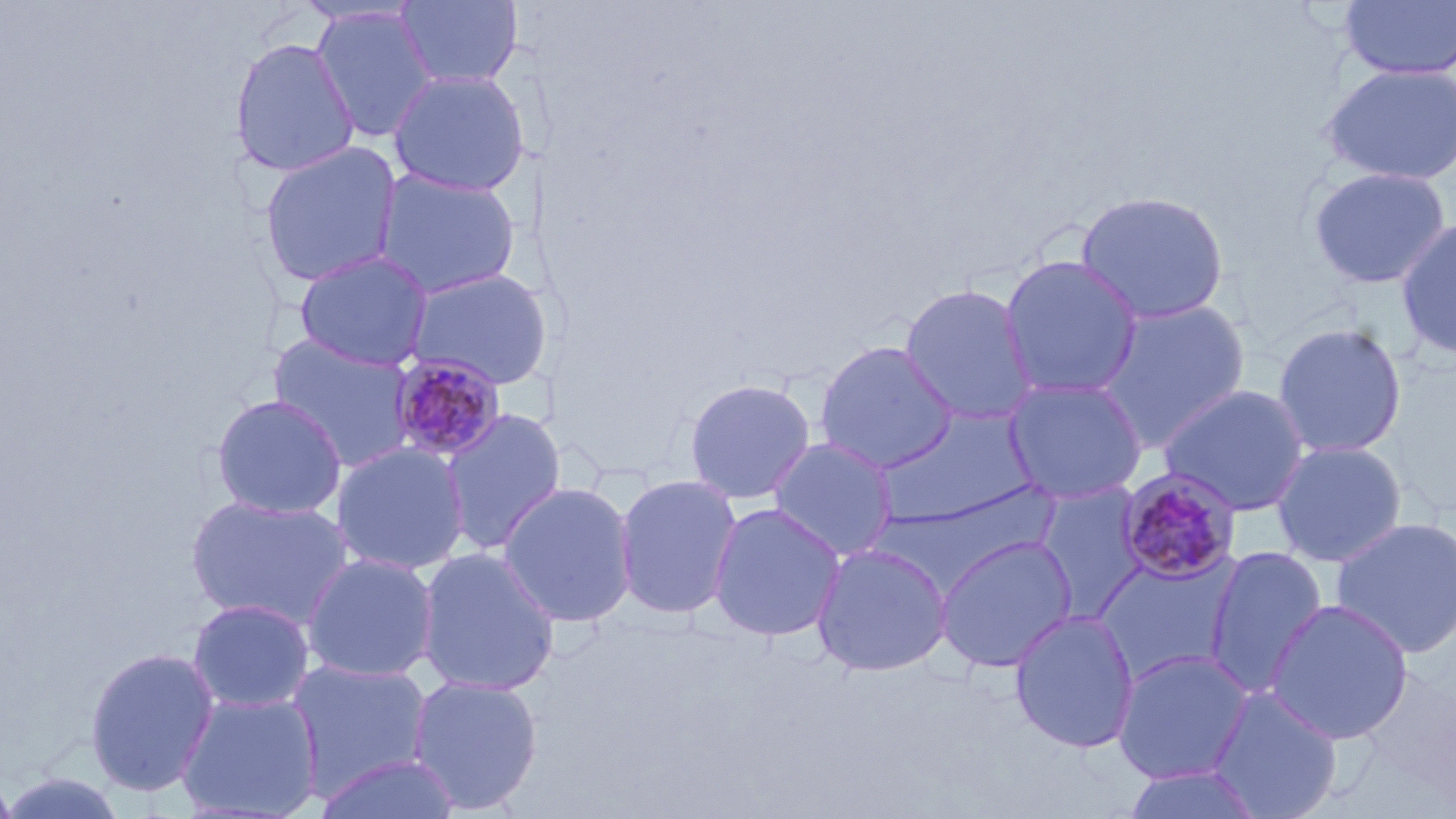
Approximate bounding boxes as named x1/y1/x2/y2 corners in pixels. Uninfected red blood cell locations: (x1=394, y1=0, x2=523, y2=89), (x1=1337, y1=1, x2=1456, y2=80), (x1=310, y1=6, x2=439, y2=143), (x1=228, y1=36, x2=359, y2=177), (x1=1318, y1=62, x2=1456, y2=186), (x1=388, y1=69, x2=530, y2=196), (x1=258, y1=141, x2=404, y2=287), (x1=1306, y1=166, x2=1453, y2=290), (x1=373, y1=168, x2=523, y2=300), (x1=1075, y1=190, x2=1230, y2=325), (x1=1395, y1=216, x2=1456, y2=360), (x1=293, y1=250, x2=434, y2=371), (x1=1000, y1=254, x2=1143, y2=400), (x1=402, y1=267, x2=551, y2=390), (x1=899, y1=283, x2=1039, y2=426), (x1=1095, y1=300, x2=1250, y2=450), (x1=1272, y1=321, x2=1408, y2=459), (x1=268, y1=332, x2=420, y2=472), (x1=815, y1=340, x2=958, y2=474), (x1=683, y1=377, x2=816, y2=504), (x1=1003, y1=378, x2=1147, y2=505), (x1=1158, y1=383, x2=1312, y2=516), (x1=211, y1=394, x2=347, y2=520), (x1=877, y1=406, x2=1038, y2=527), (x1=439, y1=408, x2=567, y2=555), (x1=768, y1=437, x2=899, y2=561), (x1=1271, y1=439, x2=1408, y2=567), (x1=331, y1=441, x2=470, y2=575), (x1=613, y1=473, x2=743, y2=619), (x1=498, y1=482, x2=638, y2=627), (x1=1033, y1=483, x2=1148, y2=620), (x1=186, y1=494, x2=352, y2=630), (x1=707, y1=502, x2=846, y2=642), (x1=1330, y1=516, x2=1456, y2=659), (x1=933, y1=534, x2=1078, y2=673), (x1=811, y1=542, x2=953, y2=677), (x1=1204, y1=545, x2=1329, y2=697), (x1=415, y1=547, x2=561, y2=696), (x1=301, y1=552, x2=440, y2=683), (x1=1092, y1=553, x2=1243, y2=682), (x1=188, y1=598, x2=315, y2=713), (x1=1265, y1=598, x2=1415, y2=745), (x1=1008, y1=609, x2=1141, y2=754), (x1=84, y1=646, x2=220, y2=797), (x1=1112, y1=649, x2=1255, y2=783), (x1=286, y1=657, x2=435, y2=799), (x1=407, y1=675, x2=544, y2=814), (x1=1208, y1=686, x2=1343, y2=819), (x1=176, y1=691, x2=324, y2=819), (x1=311, y1=752, x2=464, y2=818), (x1=1120, y1=764, x2=1268, y2=818), (x1=0, y1=765, x2=19, y2=819), (x1=2, y1=770, x2=130, y2=818). Plasmodium malariae-infected red blood cell locations: (x1=388, y1=353, x2=506, y2=462), (x1=1115, y1=468, x2=1243, y2=585). Slide-level diagnosis: Plasmodium malariae. May-Grünwald-Giemsa-stained preparation. Light microscopy. One field of a larger specimen. Thin blood film. Image is 1456×819 pixels. 1000x magnification.